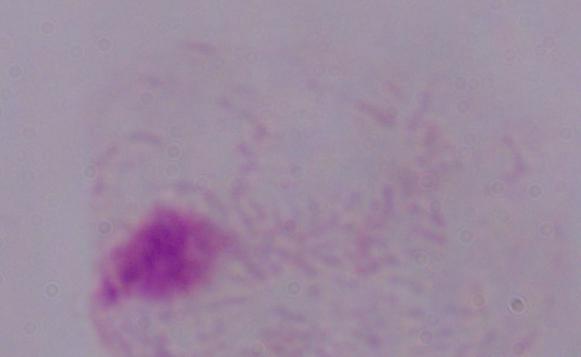
Summary:
  - Modality: micrograph
  - Identification: trichomonad
  - Magnification: 1000x